Name the parasite shown.
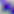

This is Toxoplasma gondii.

Captured at 400x magnification. Micrograph.